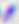
Micrograph. 400x magnification. Toxoplasma gondii is shown.